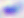
Summary:
  - Magnification: 400x
  - Identification: Toxoplasma gondii
  - Modality: photomicrograph